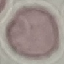
Summary:
  - Result: no malaria parasites detected
  - Preparation: thin blood smear
  - Image type: automatically extracted cell patch, resized to 64 × 64 pixels
  - Capture: smartphone camera at the microscope eyepiece
  - Stain: Giemsa